Assess this cell for malaria.
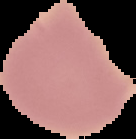
It is uninfected.

The area outside the segmented cell region is set to black. Image is 136×139 pixels. From a thin blood film.